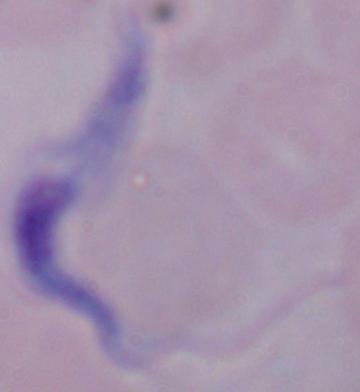

modality: photomicrograph
identification: trypanosome
magnification: 1000x